Assess for Plasmodium parasites.
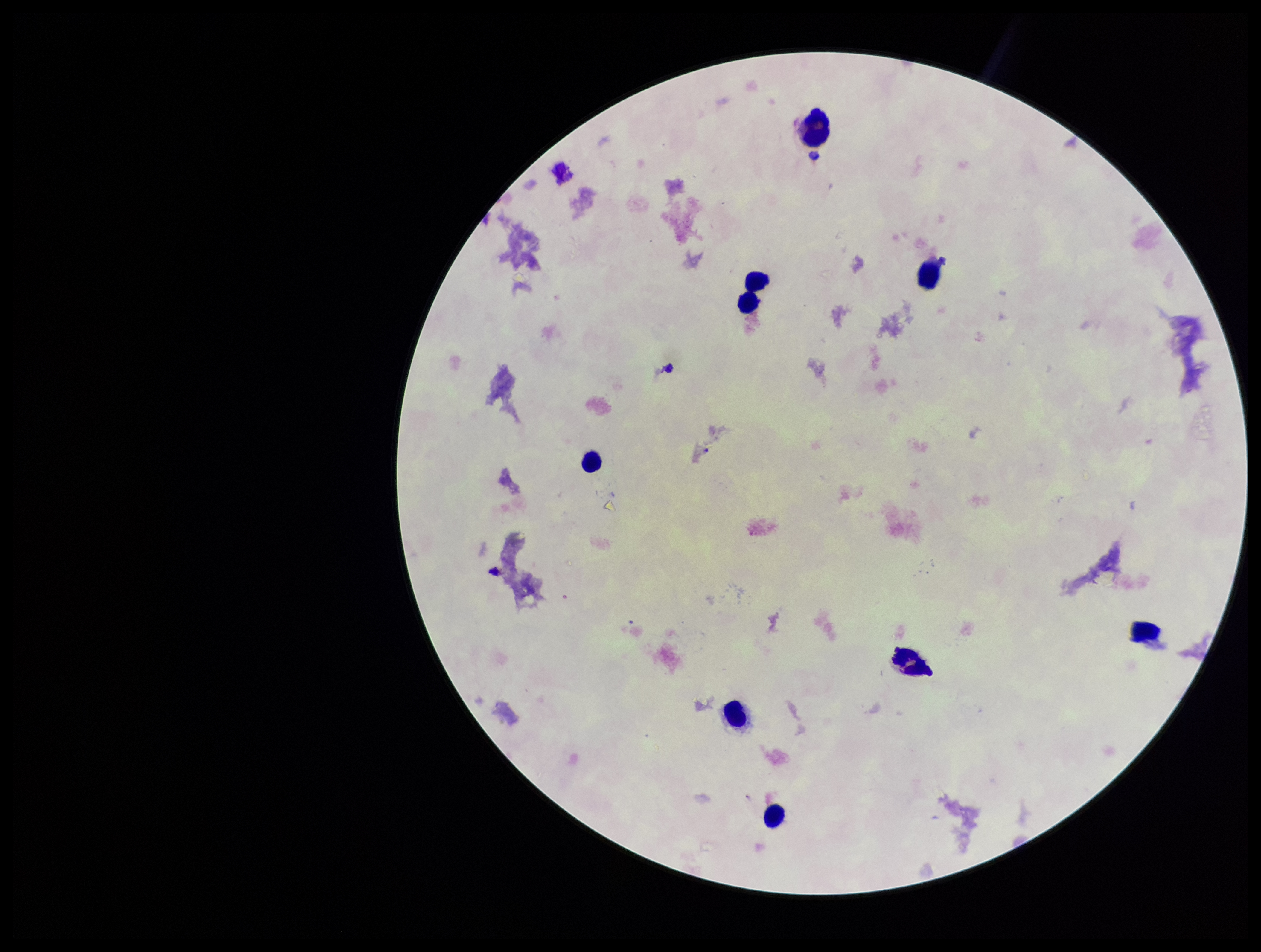
None identified.

parasite_count: 0
field_of_view: single
patient_malaria_status: negative
capture: smartphone photograph through the microscope eyepiece
leukocyte_count: 9
image_size: 1261×952 pixels
preparation: thick
stain: Giemsa